Name the parasite shown.
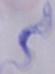

A trypanosome.

1000x magnification. Micrograph.